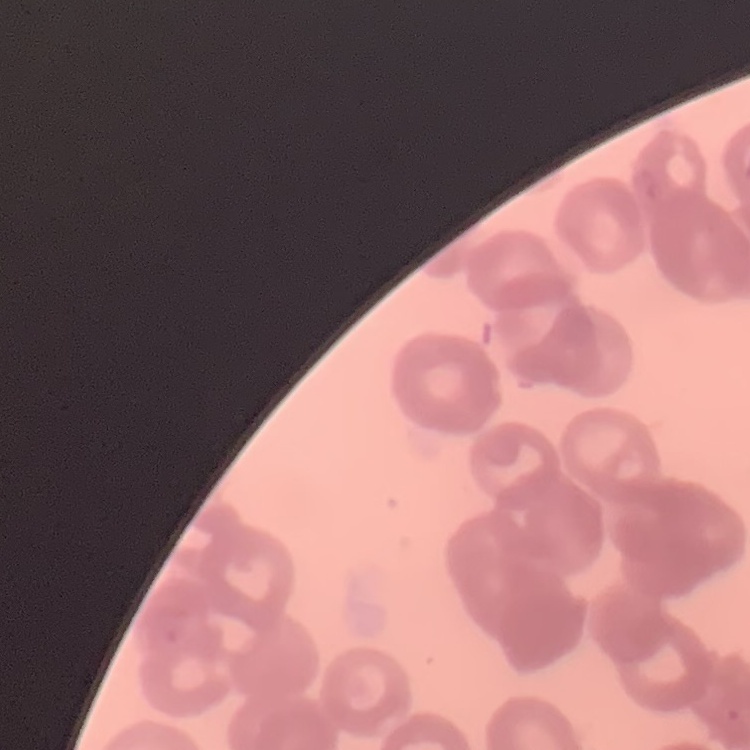

red blood cell morphology = rouleaux formation
stain = Field's or Giemsa
preparation = thin blood smear
image type = square crop of a larger photomicrograph